Point out each leukocyte.
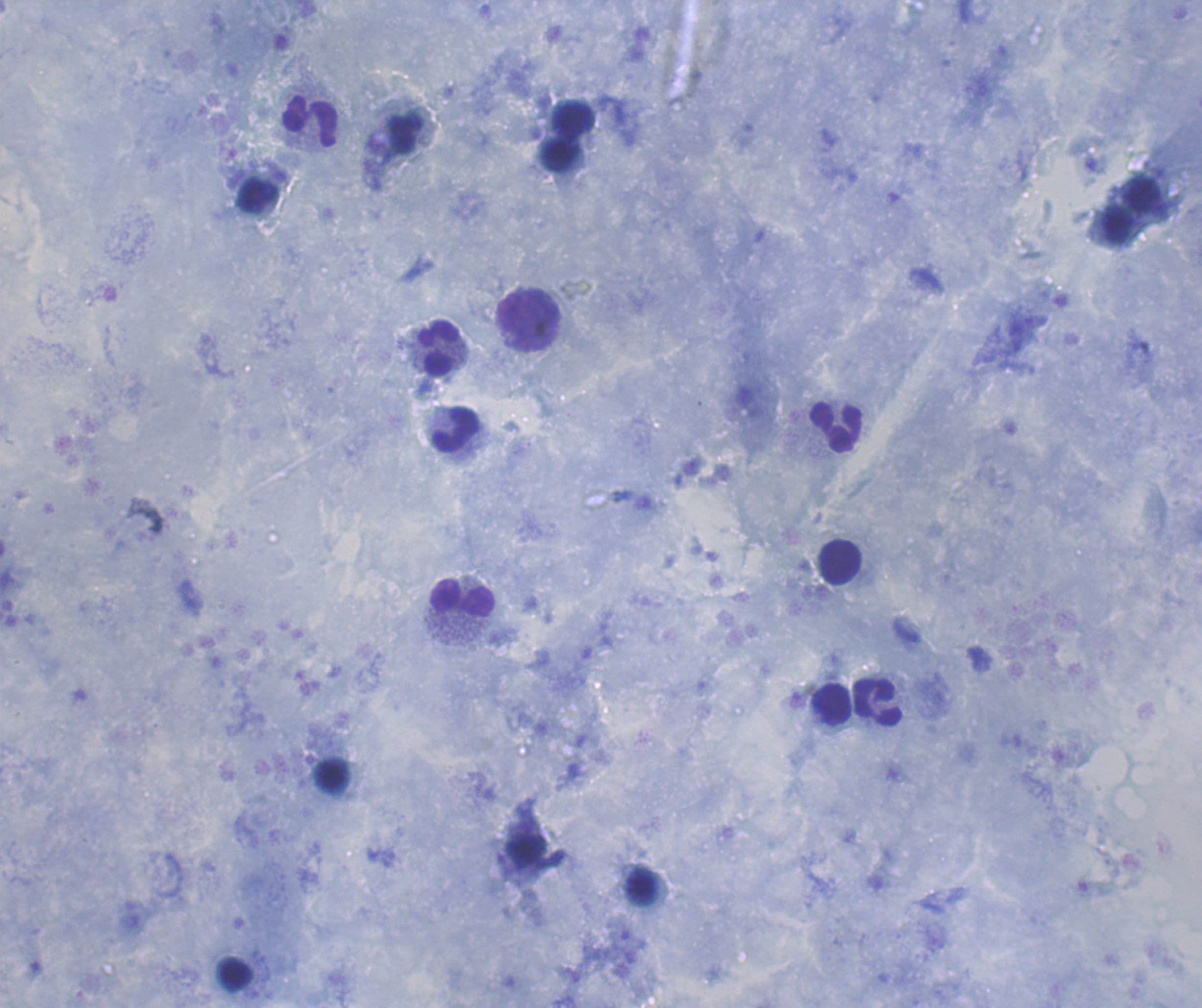
Approximate centers as [x, y] in pixels.
Leukocytes: [573, 120], [310, 121], [562, 157], [257, 195], [1143, 196], [1117, 225], [529, 321], [439, 348], [835, 427], [456, 428], [840, 563], [462, 598], [877, 703], [831, 704], [332, 775], [640, 888], [235, 975].

Result: negative for malaria parasites. Coloration quality: good. Captured at 100x magnification. Thick blood film. Previously used in an actual diagnosis. Background quality: satisfactory. Image is 1202×1008 pixels. Romanowsky-stained preparation. One field from this slide.